Describe the morphology of the erythrocytes.
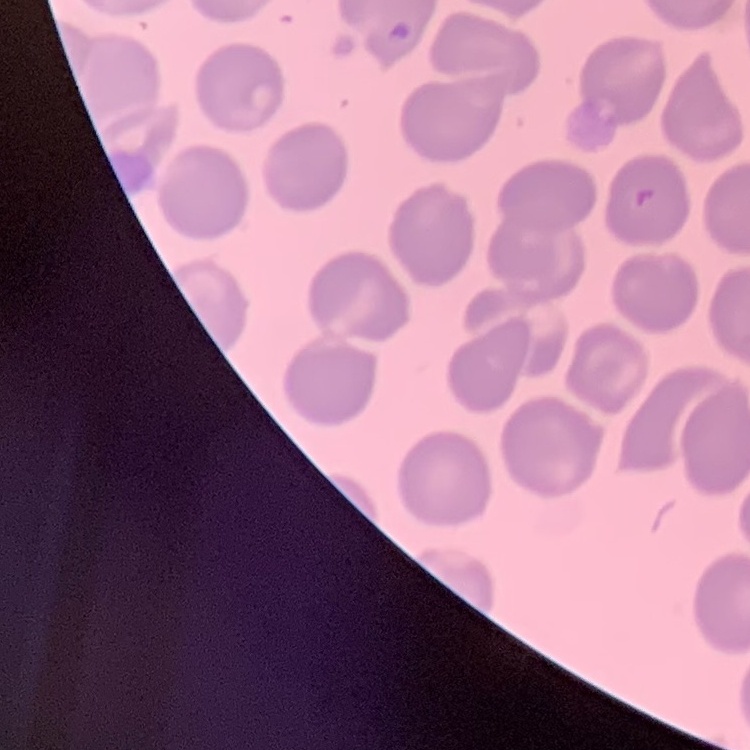

They show no rouleaux formation.

Summary:
  - Image type: one tile cut from a larger photomicrograph
  - Preparation: thin peripheral smear
  - Stain: Field's or Giemsa